Locate every leukocyte (white blood cell).
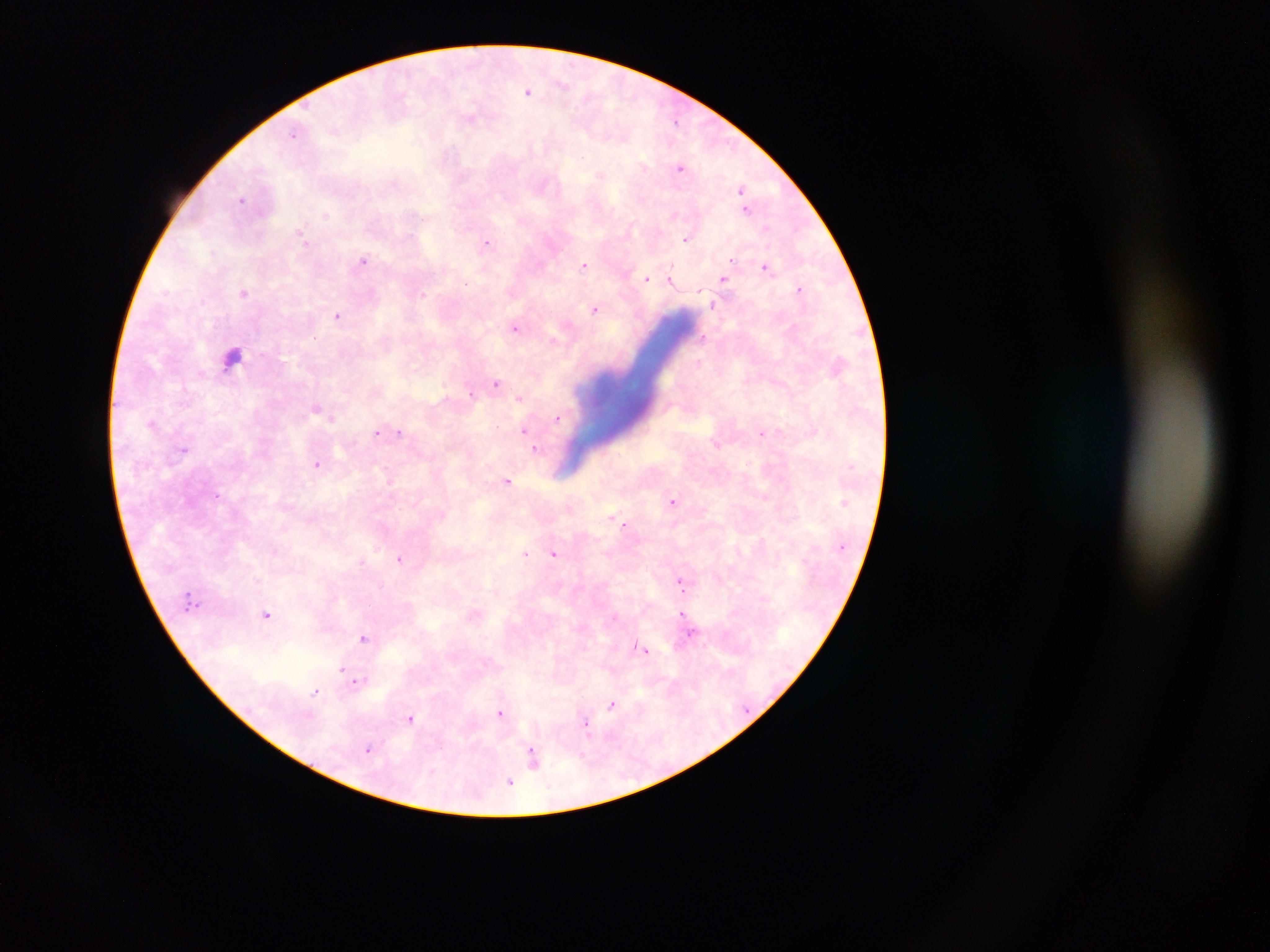
Approximate centers as x y in pixels.
Leukocytes: 232 358.

malaria parasite locations = approximate centers as x y in pixels: 563 84; 528 91; 470 118; 676 120; 293 134; 581 158; 681 168; 600 175; 742 189; 242 199; 745 210; 674 214; 326 215; 766 229; 302 234; 686 239; 487 243; 732 259; 363 260; 583 265; 767 268; 648 279; 723 279; 671 281; 466 284; 800 287; 245 293; 422 293; 713 305; 595 308; 338 316; 515 327; 703 336; 554 340; 698 362; 496 383; 472 393; 520 397; 317 410; 327 415; 332 417; 557 419; 152 423; 524 429; 399 431; 377 432; 762 433; 183 449; 536 449; 317 464; 387 476; 507 481; 673 500; 615 518; 621 521; 624 524; 525 553; 554 554; 400 559; 362 561; 681 581; 381 586; 266 614; 682 614; 691 634; 364 638; 640 648; 341 670; 357 682; 316 691; 612 705; 500 713; 410 718; 585 725; 368 749; 533 757; 510 782
country = Ghana
preparation = thick blood smear
image size = 1270×952 pixels
capture = mobile-phone photograph through a microscope
field of view = single